Describe the morphology of the erythrocytes.
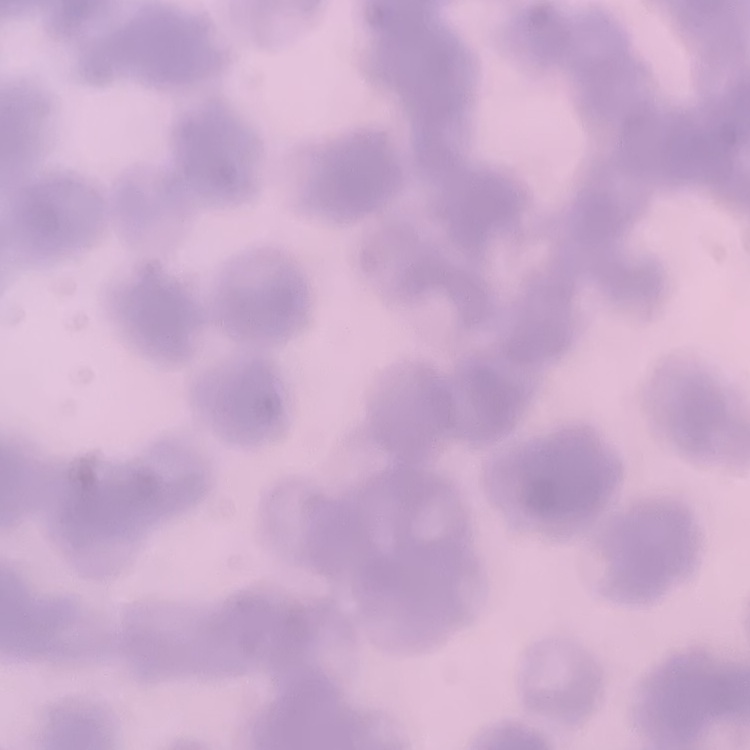

They show rouleaux formation.

Summary:
  - Stain: Field's or Giemsa
  - Image type: one tile cut from a larger photomicrograph
  - Preparation: thin peripheral smear